Name the blood parasite species.
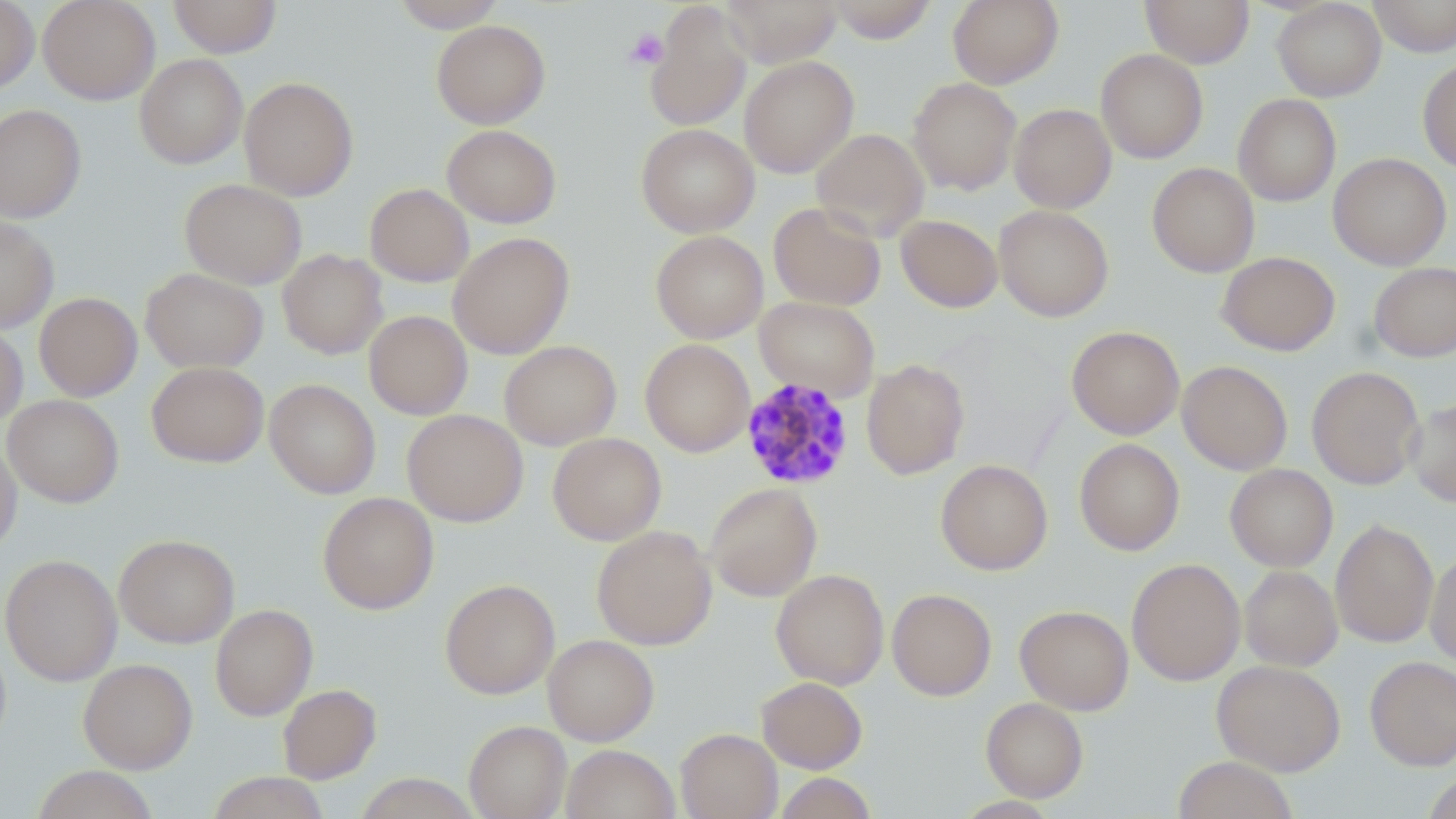
Plasmodium malariae.

Summary:
  - Coordinate format: approximate bounding boxes as (x1, y1, x2, y2) in pixels
  - Uninfected red blood cell locations: (0, 0, 39, 94), (38, 0, 160, 104), (169, 0, 281, 58), (389, 0, 507, 31), (719, 0, 842, 67), (947, 0, 1064, 89), (1140, 0, 1254, 67), (1272, 0, 1386, 101), (1368, 0, 1456, 57), (826, 1, 938, 43), (644, 3, 752, 133), (432, 20, 550, 129), (1095, 49, 1208, 163), (134, 54, 248, 169), (739, 56, 858, 178), (1418, 60, 1456, 174), (239, 76, 359, 200), (908, 77, 1022, 195), (1233, 94, 1341, 206), (0, 103, 86, 222), (1009, 103, 1116, 213), (636, 123, 759, 237), (442, 124, 562, 228), (811, 128, 929, 241), (1328, 152, 1452, 270), (1147, 162, 1259, 277), (179, 178, 307, 289), (365, 183, 474, 286), (768, 202, 886, 311), (994, 205, 1114, 322), (896, 215, 1002, 313), (0, 216, 59, 332), (651, 230, 768, 343), (448, 232, 574, 359), (277, 249, 387, 359), (1217, 251, 1340, 356), (1369, 262, 1456, 361), (141, 267, 268, 373), (34, 292, 142, 401), (755, 297, 880, 401), (364, 311, 472, 420), (0, 320, 28, 428), (1066, 325, 1185, 439), (640, 339, 755, 457), (499, 340, 621, 450), (861, 359, 970, 480), (1177, 360, 1293, 475), (147, 361, 268, 467), (1307, 366, 1424, 490), (148, 371, 382, 477), (264, 379, 381, 498), (2, 394, 124, 507), (1406, 398, 1456, 507), (403, 409, 528, 526), (547, 432, 666, 545), (0, 436, 22, 557), (1074, 438, 1185, 556), (936, 460, 1052, 575), (1225, 464, 1338, 571), (705, 482, 822, 602), (318, 492, 439, 614), (1330, 518, 1439, 648), (592, 525, 717, 650), (114, 533, 239, 648), (1426, 549, 1456, 667), (1, 554, 123, 686), (1126, 558, 1245, 686), (1239, 565, 1343, 671), (770, 569, 889, 689), (440, 578, 560, 699), (887, 588, 997, 701), (210, 604, 317, 720), (1015, 605, 1134, 715), (542, 634, 659, 745), (1365, 655, 1456, 770), (79, 658, 197, 773), (1212, 659, 1345, 775), (756, 676, 868, 773), (277, 683, 381, 783), (981, 697, 1089, 802), (464, 720, 571, 819), (676, 728, 782, 819), (561, 744, 680, 819), (1173, 756, 1296, 819), (31, 766, 158, 819), (1423, 771, 1456, 819), (207, 772, 330, 818), (354, 773, 480, 818), (775, 773, 878, 819)
  - Plasmodium malariae-infected red blood cell locations: (741, 377, 855, 490)
  - Platelet locations: (624, 28, 669, 70)
  - Modality: light microscopy
  - Magnification: 1000x
  - Preparation: thin blood smear
  - Stain: May-Grünwald-Giemsa
  - Field of view: one of a larger specimen
  - Image size: 1456×819 pixels